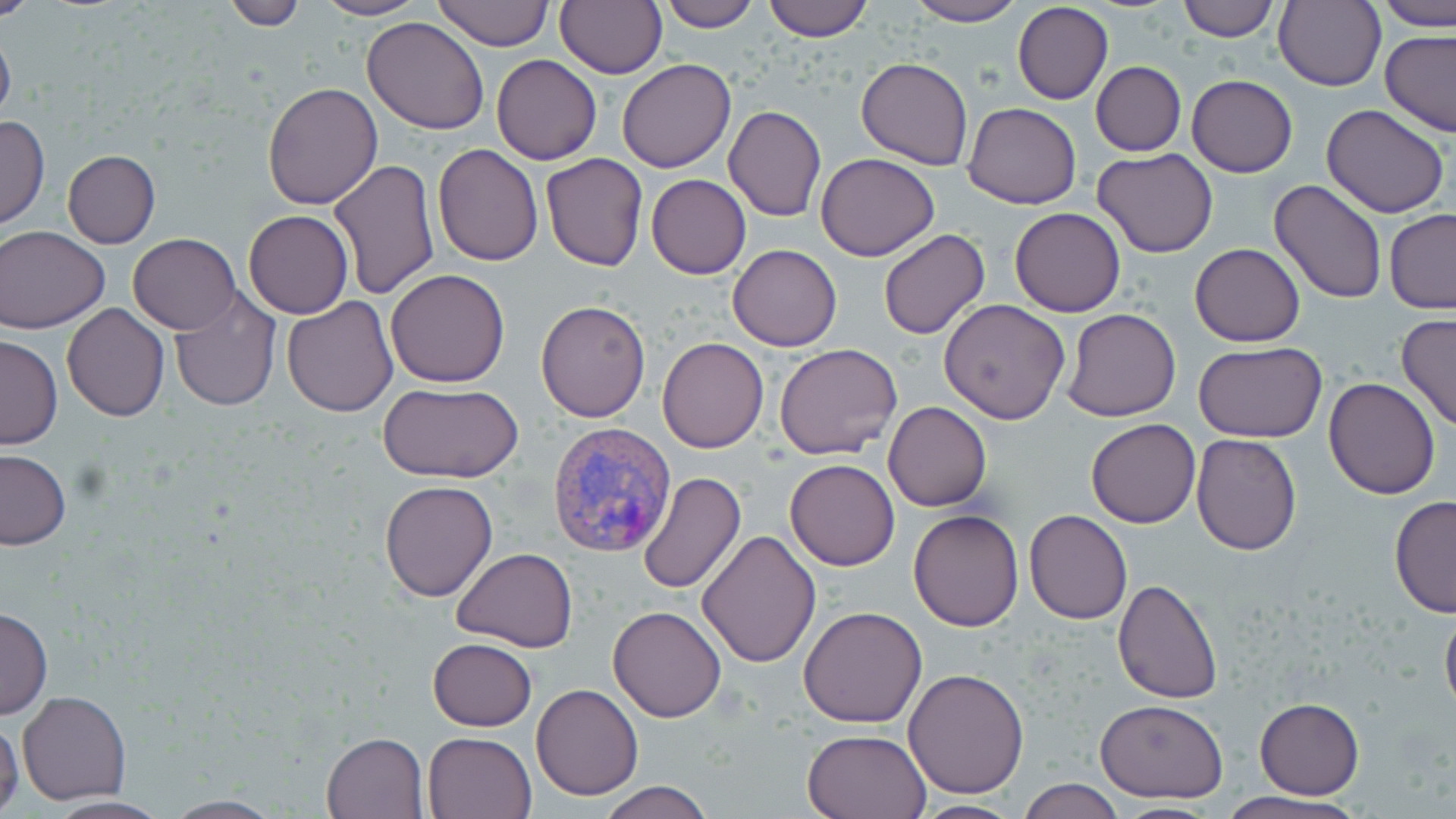 Approximate bounding boxes as (x1, y1, x2, y2) in pixels. Uninfected red blood cell locations: (0, 0, 39, 21), (312, 0, 425, 21), (555, 0, 667, 79), (659, 0, 760, 31), (763, 0, 873, 41), (902, 0, 1025, 26), (1174, 0, 1280, 41), (1376, 0, 1456, 31), (219, 1, 305, 29), (432, 1, 552, 49), (1273, 1, 1385, 90), (1012, 2, 1113, 104), (362, 16, 491, 135), (0, 22, 16, 132), (1381, 30, 1456, 137), (492, 54, 602, 165), (856, 57, 974, 170), (617, 58, 736, 173), (1091, 61, 1186, 156), (1187, 74, 1297, 177), (262, 82, 382, 210), (963, 101, 1081, 209), (1321, 102, 1450, 219), (722, 105, 826, 221), (0, 115, 50, 229), (432, 144, 543, 265), (1092, 148, 1219, 257), (63, 150, 161, 248), (816, 152, 940, 260), (540, 154, 649, 272), (329, 160, 439, 298), (646, 174, 750, 279), (1268, 178, 1390, 304), (1008, 206, 1126, 316), (1384, 209, 1456, 312), (243, 211, 352, 320), (1, 225, 109, 334), (877, 229, 990, 341), (129, 234, 240, 334), (1188, 243, 1306, 346), (727, 244, 842, 351), (386, 269, 511, 387), (168, 288, 281, 412), (281, 296, 397, 417), (939, 299, 1072, 424), (536, 300, 650, 422), (62, 303, 169, 422), (1062, 309, 1182, 423), (1397, 313, 1456, 433), (1, 335, 63, 450), (657, 337, 768, 453), (1194, 342, 1327, 443), (774, 343, 904, 461), (1323, 376, 1441, 500), (378, 383, 522, 485), (883, 401, 992, 511), (1086, 418, 1200, 529), (1190, 434, 1302, 555), (0, 450, 71, 550), (785, 459, 900, 571), (636, 471, 747, 596), (380, 480, 497, 602), (1389, 494, 1456, 618), (909, 508, 1024, 632), (1023, 509, 1132, 624), (695, 529, 822, 669), (451, 546, 578, 652), (1113, 577, 1224, 704), (1440, 603, 1456, 720), (0, 605, 53, 721), (607, 605, 727, 722), (799, 606, 928, 729), (427, 638, 536, 732), (904, 668, 1029, 797), (532, 683, 644, 800), (19, 691, 131, 805), (1094, 698, 1229, 802), (1255, 698, 1364, 799), (0, 719, 23, 819), (801, 728, 931, 818), (322, 731, 429, 818), (423, 731, 537, 819), (1017, 778, 1124, 819), (598, 780, 714, 819), (1215, 792, 1362, 819), (41, 794, 175, 818), (157, 794, 289, 818), (908, 799, 1026, 817), (1102, 802, 1229, 817). Plasmodium vivax-infected red blood cell locations: (546, 422, 678, 560). Slide-level diagnosis: Plasmodium vivax. 1000x magnification. One field of a larger specimen. Image is 1456×819 pixels. Thin blood film. Optical microscopy. May-Grünwald-Giemsa stain.